Classify this cell by malaria status.
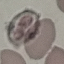

It is uninfected.

{
  "image_type": "automatically extracted cell patch, resized to 64 × 64 pixels",
  "preparation": "thin smear",
  "capture": "smartphone camera at the microscope eyepiece",
  "stain": "Giemsa"
}